Outline each uninfected red blood cell.
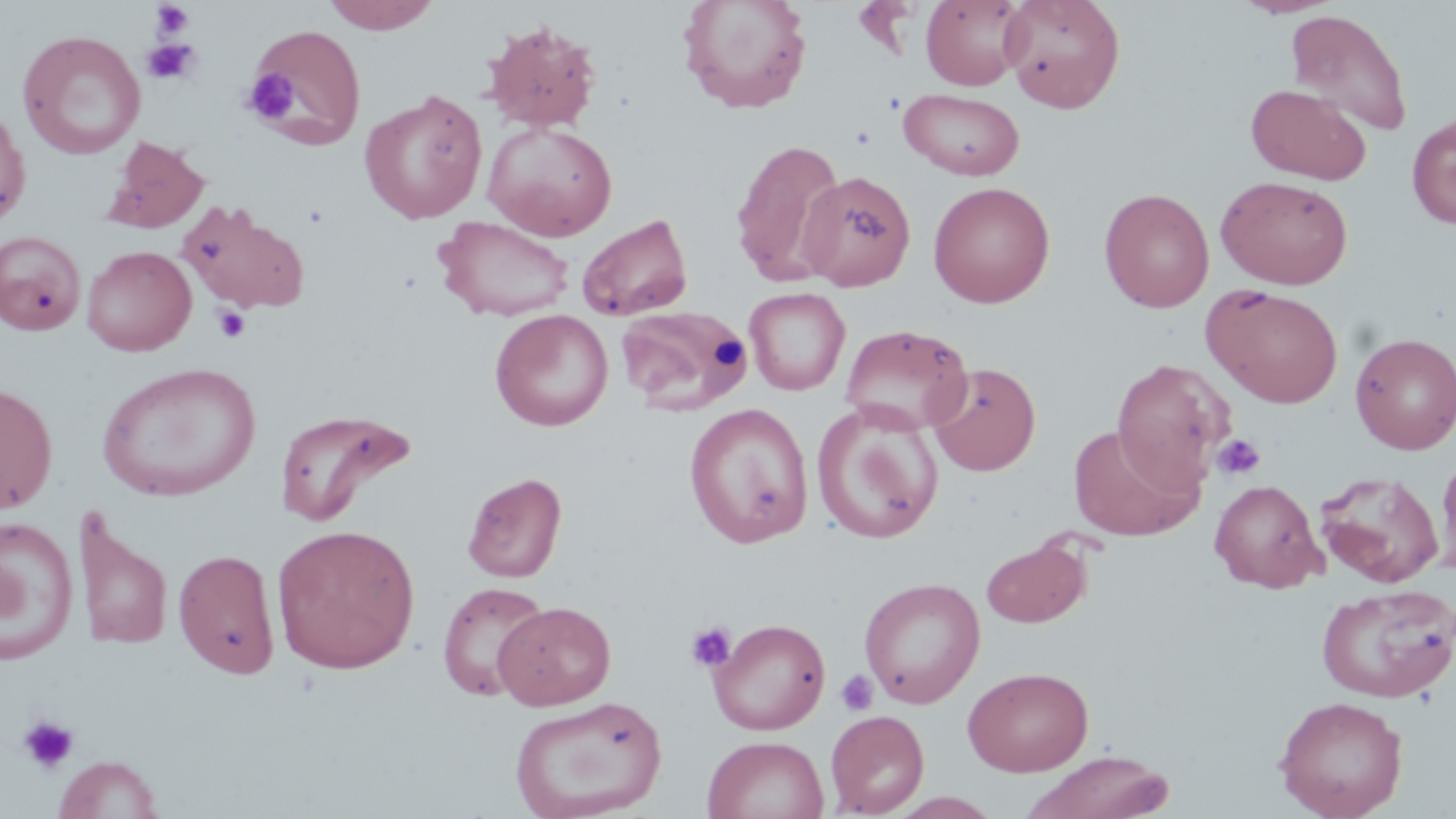

Approximate bounding boxes as (x1, y1, x2, y2) in pixels.
Uninfected red blood cells: (322, 0, 440, 33), (921, 0, 1029, 90), (1000, 0, 1126, 112), (1232, 0, 1343, 18), (677, 1, 814, 114), (1285, 9, 1413, 137), (481, 19, 602, 134), (247, 23, 367, 149), (17, 30, 146, 160), (1245, 84, 1371, 184), (360, 88, 487, 224), (899, 88, 1024, 180), (0, 104, 31, 229), (1407, 114, 1456, 229), (482, 121, 618, 241), (101, 135, 210, 233), (730, 137, 847, 286), (798, 170, 915, 291), (1216, 175, 1354, 289), (928, 181, 1055, 308), (1098, 187, 1215, 312), (178, 200, 309, 313), (576, 213, 694, 321), (435, 216, 575, 322), (0, 230, 87, 336), (82, 245, 197, 356), (1203, 285, 1344, 409), (744, 287, 850, 396), (615, 304, 754, 414), (489, 309, 614, 431), (840, 323, 973, 435), (1350, 332, 1456, 454), (1111, 359, 1234, 489), (926, 361, 1041, 476), (97, 362, 260, 502), (0, 381, 58, 514), (684, 402, 814, 548), (812, 402, 944, 545), (274, 407, 416, 527), (1067, 423, 1203, 542), (1437, 453, 1456, 578), (462, 471, 567, 583), (1315, 471, 1445, 588), (1209, 479, 1326, 593), (72, 507, 172, 654), (0, 515, 80, 666), (271, 523, 421, 675), (981, 538, 1090, 629), (173, 547, 280, 678), (859, 576, 985, 709), (437, 581, 551, 703), (1317, 583, 1455, 704), (494, 601, 616, 710), (708, 617, 831, 735), (963, 666, 1094, 775), (510, 695, 667, 819), (1274, 695, 1409, 819), (825, 709, 929, 817), (702, 734, 829, 819), (1022, 750, 1177, 819), (53, 754, 164, 819).

slide_level_diagnosis: no evidence of blood parasites
magnification: 1000x
image_size: 1456×819 pixels
preparation: thin blood film
field_of_view: single
platelet_locations: 'approximate bounding boxes as (x1, y1, x2, y2) in pixels: (150, 2, 195, 40), (141, 38, 201, 85), (244, 70, 300, 123), (212, 303, 251, 344), (1211, 433, 1266, 480), (684, 621, 736, 672), (836, 669, 879, 716), (16, 714, 80, 775)'
stain: May-Grünwald-Giemsa
modality: light microscopy